Assess this cell for malaria.
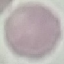
Uninfected.

Automatically extracted cell patch, resized to 64 × 64 pixels. Thin blood film. Photographed with a smartphone camera at the microscope eyepiece. Giemsa stain.